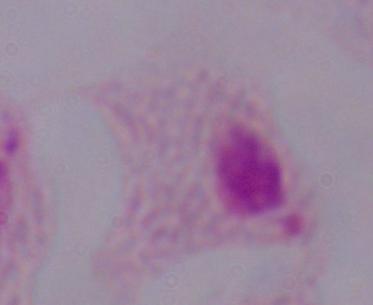 1000x magnification. A trichomonad is shown. Micrograph.